Give the preparation type.
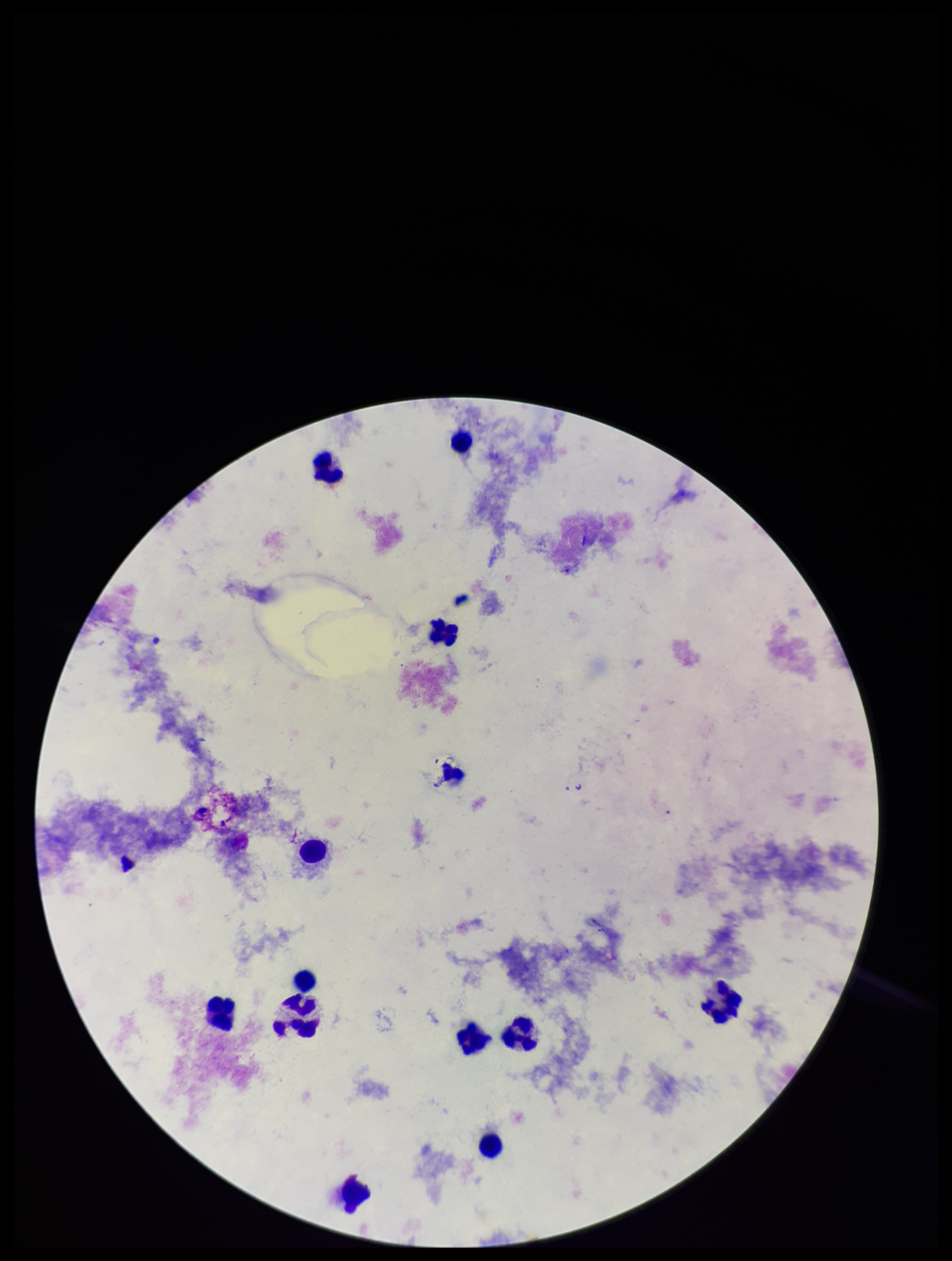

Thick.

Summary:
  - Plasmodium parasites: none seen
  - Field of view: single
  - Parasite count: 0
  - Patient malaria status: negative
  - Image size: 952×1261 pixels
  - Capture: smartphone photograph through the microscope eyepiece
  - Leukocyte count: 12
  - Stain: Giemsa